Name the blood parasite species.
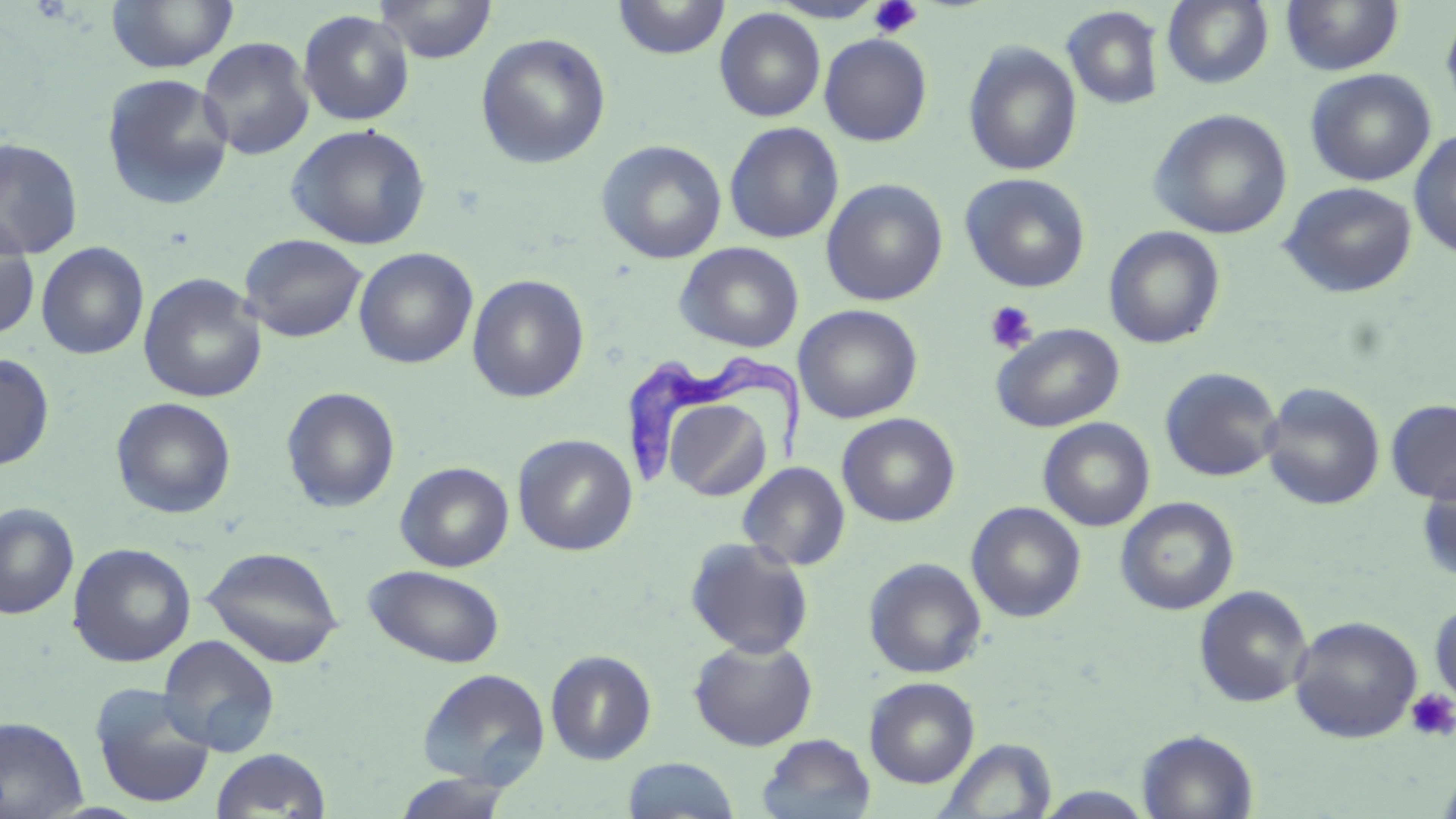

Trypanosoma brucei.

Approximate bounding boxes as [x1, y1, x2, y2] in pixels. Trypanosoma brucei locations: [620, 357, 812, 497]. Uninfected red blood cell locations: [105, 0, 238, 73], [373, 0, 497, 64], [612, 0, 730, 60], [769, 0, 885, 23], [1162, 0, 1274, 89], [1281, 0, 1404, 76], [1440, 3, 1456, 123], [1062, 6, 1165, 109], [714, 7, 825, 122], [297, 10, 414, 126], [475, 32, 611, 169], [819, 33, 932, 146], [197, 37, 315, 160], [963, 41, 1082, 177], [1305, 69, 1436, 186], [100, 73, 234, 210], [1149, 108, 1293, 240], [724, 122, 844, 244], [287, 123, 430, 250], [1409, 130, 1456, 259], [0, 138, 83, 259], [596, 140, 727, 264], [960, 173, 1091, 293], [821, 178, 948, 306], [1279, 182, 1417, 298], [0, 219, 40, 339], [1103, 226, 1226, 349], [240, 234, 368, 343], [36, 242, 148, 360], [675, 242, 804, 353], [354, 247, 477, 369], [138, 273, 266, 403], [467, 275, 590, 403], [794, 305, 923, 424], [991, 323, 1125, 433], [0, 353, 55, 471], [1160, 367, 1282, 482], [1260, 382, 1385, 511], [281, 387, 401, 512], [111, 397, 236, 518], [662, 397, 774, 502], [1385, 399, 1456, 504], [836, 413, 960, 527], [1038, 417, 1155, 531], [513, 434, 637, 556], [395, 461, 514, 573], [738, 461, 851, 570], [1416, 469, 1456, 583], [1116, 497, 1240, 615], [966, 502, 1086, 623], [0, 503, 78, 619], [684, 537, 815, 659], [67, 542, 196, 667], [202, 545, 345, 668], [863, 557, 987, 678], [363, 564, 505, 668], [1193, 586, 1313, 708], [1429, 599, 1456, 709], [1290, 615, 1422, 743], [157, 634, 280, 757], [689, 637, 818, 751], [545, 650, 657, 765], [418, 667, 550, 789], [864, 676, 980, 788], [90, 686, 217, 809], [0, 716, 87, 818], [1136, 729, 1258, 818], [756, 733, 875, 819], [939, 738, 1056, 819], [211, 748, 331, 818], [621, 757, 739, 818], [1437, 764, 1456, 819], [393, 773, 514, 819], [1036, 786, 1154, 818]. Platelet locations: [868, 0, 923, 38], [984, 301, 1038, 355], [1406, 688, 1456, 741]. Thin blood smear. Optical microscopy. 1000x magnification. May-Grünwald-Giemsa stain. Image is 1456×819 pixels. Single field of view.